Name the parasite shown.
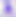

This is Toxoplasma gondii.

400x magnification. Photomicrograph.